Outline each Plasmodium falciparum parasite and classify it by life-cycle stage.
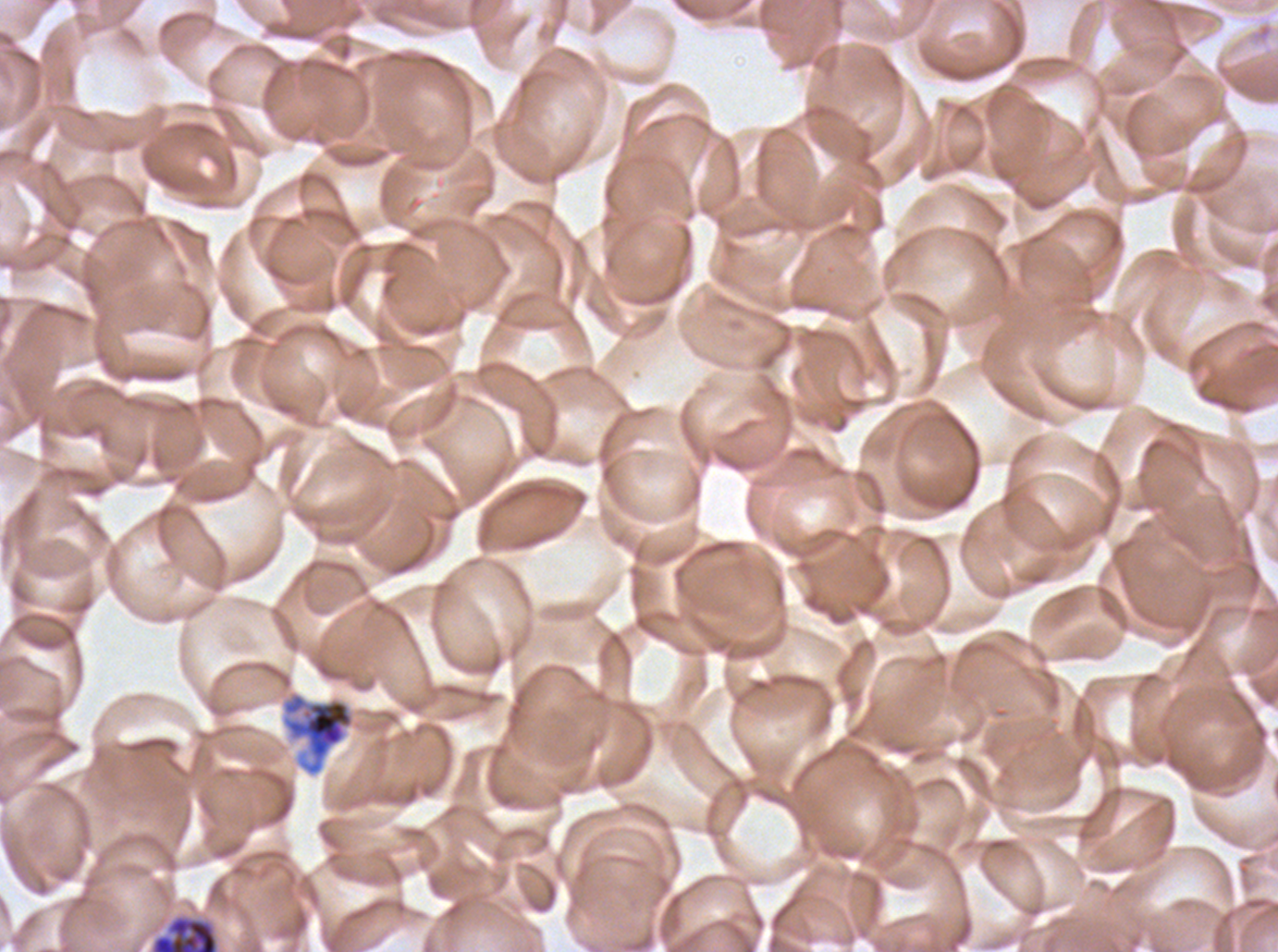

Approximate bounding boxes as {x1, y1, x2, y2} in pixels.
Early schizonts: {280, 690, 356, 776}.
Late schizonts: {151, 915, 218, 951}.
No rings, late-ring/early-trophozoite forms, mid trophozoites, late trophozoites, segmenters, or gametocytes observed.

Giemsa stain. Life-cycle stages observed: early schizont, late schizont. Thin blood smear. One sub-image of a larger composite. Image is 1278×952 pixels. Plasmodium falciparum cultured ex vivo for 24 to 48 hours, from a patient in The Gambia.